Classify this cell by malaria status.
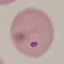
It is parasitized.

image_type: cell patch, automatically extracted from a larger field of view and resized to 64 × 64 pixels
preparation: thin blood film
stain: Giemsa
capture: smartphone camera at the microscope eyepiece